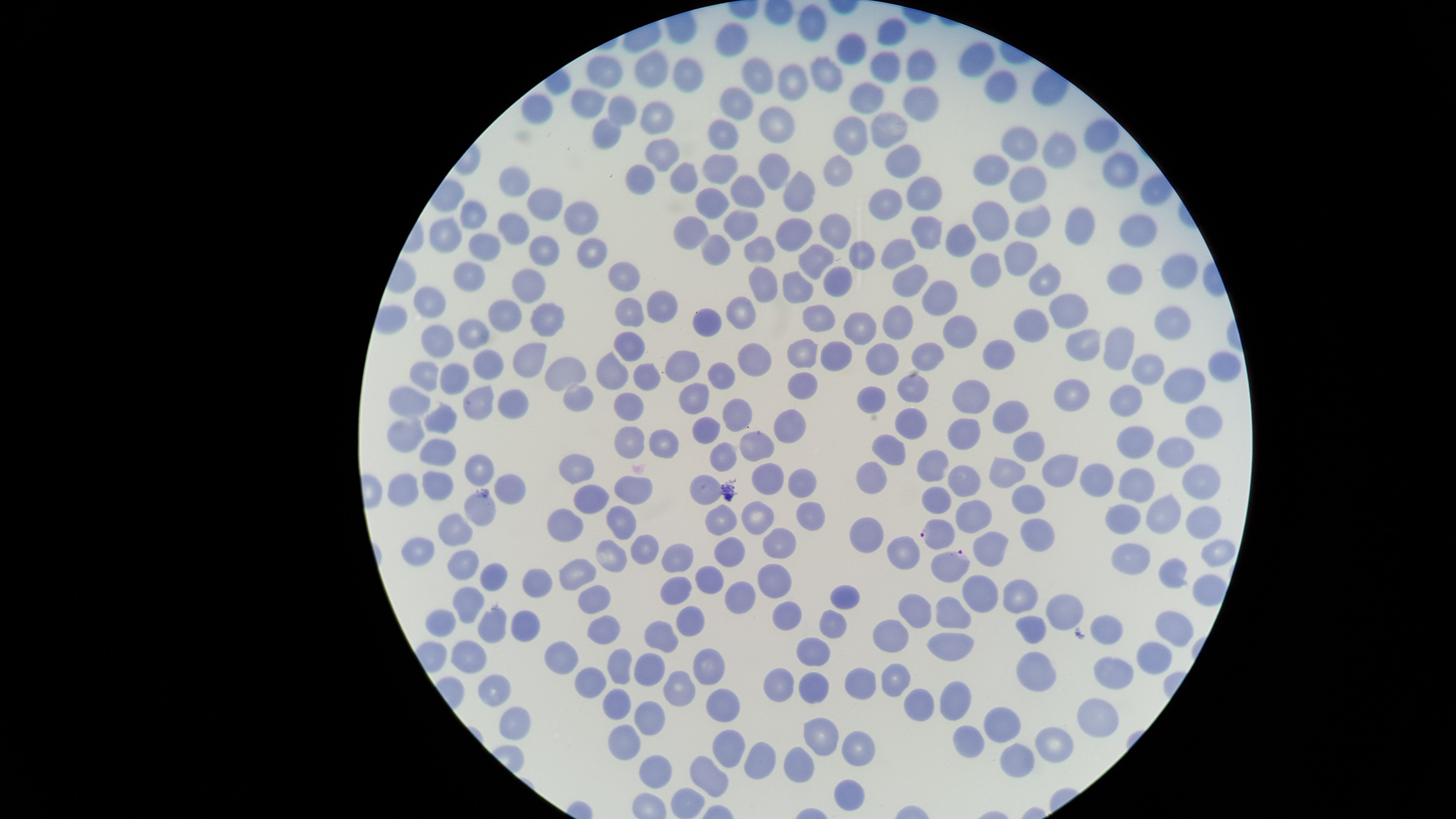 Approximate marker points as (x, y) in pixels. Uninfected red blood cells: (813, 24), (894, 33), (735, 37), (854, 47), (983, 59), (922, 61), (879, 67), (647, 69), (827, 70), (756, 72), (606, 75), (687, 77), (787, 81), (1003, 85), (866, 94), (737, 97), (596, 100), (539, 101), (914, 104), (619, 107), (655, 110), (775, 122), (602, 130), (888, 130), (722, 131), (854, 131), (1101, 132), (1016, 140), (1053, 148), (658, 152), (898, 159), (722, 163), (841, 167), (1118, 169), (990, 170), (772, 173), (681, 177), (639, 179), (1027, 180), (509, 184), (801, 184), (745, 186), (921, 197), (710, 198), (544, 204), (883, 204), (473, 209), (994, 214), (577, 217), (1034, 218), (736, 225), (1071, 226), (513, 227), (924, 227), (799, 228), (841, 228), (694, 230), (445, 233), (1137, 233), (965, 236), (716, 243), (486, 244), (757, 247), (546, 248), (586, 249), (898, 250), (862, 252), (1023, 254), (815, 258), (983, 263), (1173, 268), (619, 273), (1051, 274), (473, 276), (1124, 276), (533, 282), (799, 282), (837, 283), (910, 283), (762, 286), (940, 296), (426, 297), (661, 300), (1063, 304), (503, 307), (626, 307), (738, 307), (824, 312), (549, 316), (707, 316), (1168, 318), (896, 323), (1028, 324), (853, 330), (434, 334), (473, 334), (959, 336), (1083, 344), (1112, 345), (628, 348), (524, 350), (799, 350), (831, 354), (929, 354), (997, 356), (877, 359), (487, 363), (750, 365), (1144, 366), (1215, 366), (677, 368), (565, 369), (611, 370), (426, 374), (650, 374), (449, 377), (718, 380), (1180, 380), (805, 385), (914, 388), (575, 394), (1080, 394), (1123, 395), (871, 397), (964, 398), (695, 399), (414, 400), (479, 403), (509, 403), (629, 405), (734, 411), (1010, 415), (444, 417), (1200, 418), (907, 420), (789, 421), (403, 427), (709, 429), (963, 429), (633, 432), (663, 436), (1133, 437), (756, 443), (1176, 443), (1033, 444), (889, 446), (438, 449), (727, 458), (481, 467), (574, 467), (933, 469), (1050, 469), (765, 471), (874, 474), (1006, 474), (1101, 477), (512, 479), (1137, 480), (963, 481), (435, 482), (633, 482), (1199, 483), (408, 485), (706, 487), (799, 487), (931, 497), (595, 499), (1020, 499), (481, 509), (1161, 512), (973, 513), (758, 516), (810, 518), (621, 519), (720, 521), (1122, 522), (1203, 522), (564, 523), (863, 527), (454, 528), (1026, 535), (987, 543), (776, 545), (644, 546), (420, 547), (892, 549), (724, 551), (678, 554), (1217, 554), (603, 557), (1125, 558), (467, 566), (578, 577), (709, 577), (1165, 577), (491, 578), (773, 579), (539, 581), (675, 586), (975, 588), (737, 593), (1014, 593), (843, 594), (596, 596), (469, 600), (918, 606), (780, 607), (949, 607), (1070, 611), (687, 617), (837, 617), (444, 618), (493, 622), (1035, 624), (1102, 625), (525, 626), (601, 626), (1170, 630), (892, 633), (663, 635), (948, 642), (816, 645), (471, 651), (561, 655), (1146, 655), (710, 657), (652, 659), (1033, 660), (612, 667), (1112, 667), (812, 677), (899, 677), (864, 681), (590, 682), (779, 684), (493, 690), (680, 693), (950, 701), (616, 704), (915, 704), (724, 707), (1091, 709), (515, 714), (649, 714), (1004, 726), (974, 734), (818, 738), (618, 739), (851, 744), (1046, 744), (722, 750), (1011, 757), (760, 760), (799, 763), (653, 767), (703, 777), (845, 792). Parasitized red blood cells: (937, 533), (954, 563). Presence: malaria parasites seen. Single field of view. Giemsa-stained preparation. Thin blood film. Photographed with a smartphone camera through the microscope eyepiece. Image is 1456×819 pixels. Species: Plasmodium falciparum. The visible region is circular.